Assess this cell for malaria.
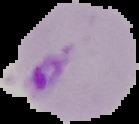

Parasitized.

image_type: segmented cell region with the area outside set to black
image_size: 139×124 pixels
preparation: thin blood smear